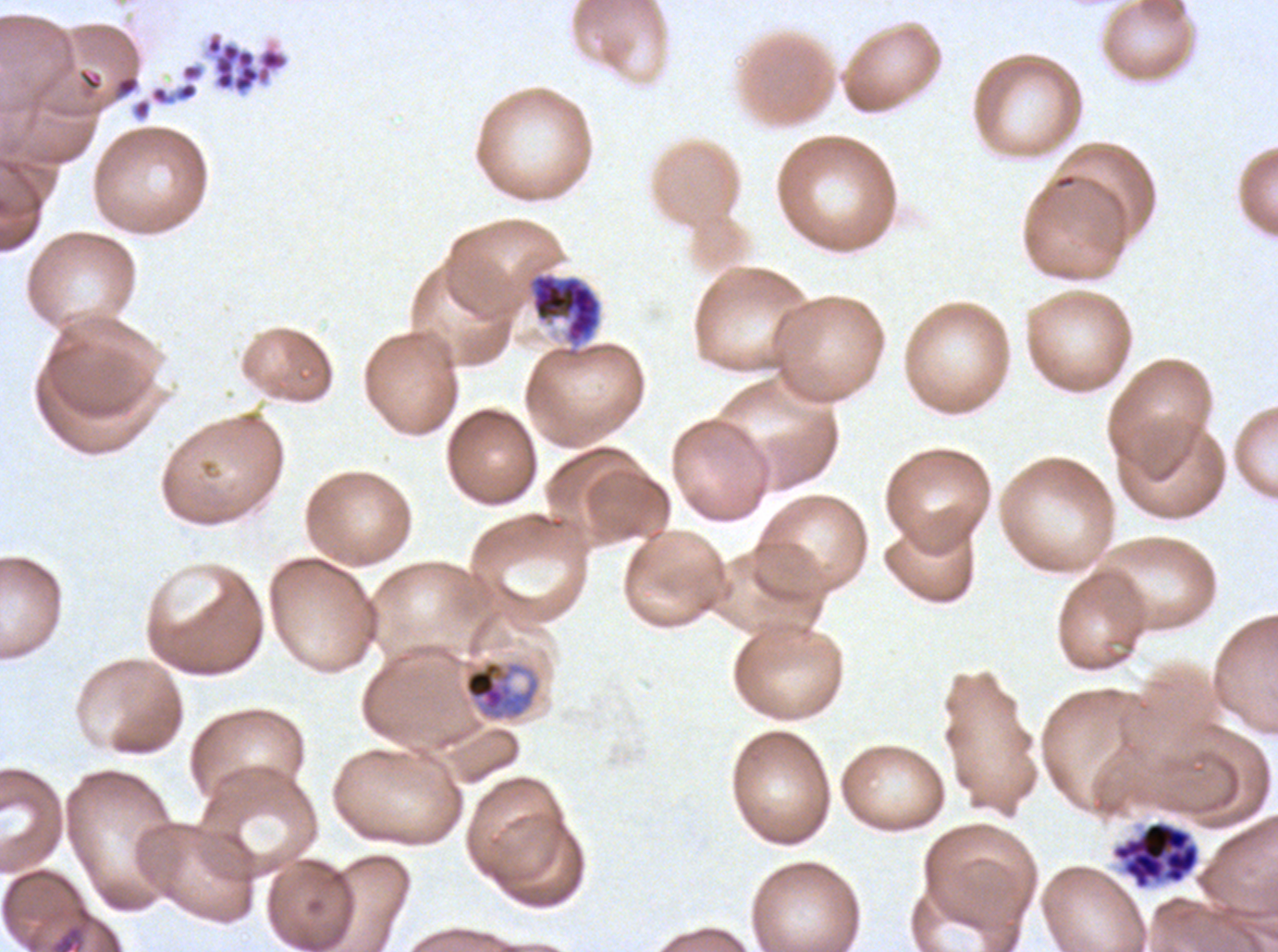
{
  "image_size": "1278×952 pixels",
  "stain": "Giemsa",
  "early_schizont_locations": "approximate bounding rectangles given as corner coordinates in pixels from the top-left: (x1=527, y1=272, x2=602, y2=348)",
  "preparation": "thin blood smear",
  "late_trophozoite_locations": "approximate bounding rectangles given as corner coordinates in pixels from the top-left: (x1=462, y1=659, x2=541, y2=722)",
  "specimen": "P. falciparum cultured ex vivo for 24 to 48 hours, from a patient in The Gambia",
  "segmenter_locations": "approximate bounding rectangles given as corner coordinates in pixels from the top-left: (x1=200, y1=29, x2=291, y2=99), (x1=1110, y1=818, x2=1201, y2=892)",
  "life_cycle_stages_observed": "late trophozoite, early schizont, segmenter",
  "field_of_view": "sub-image separated from a larger composite"
}